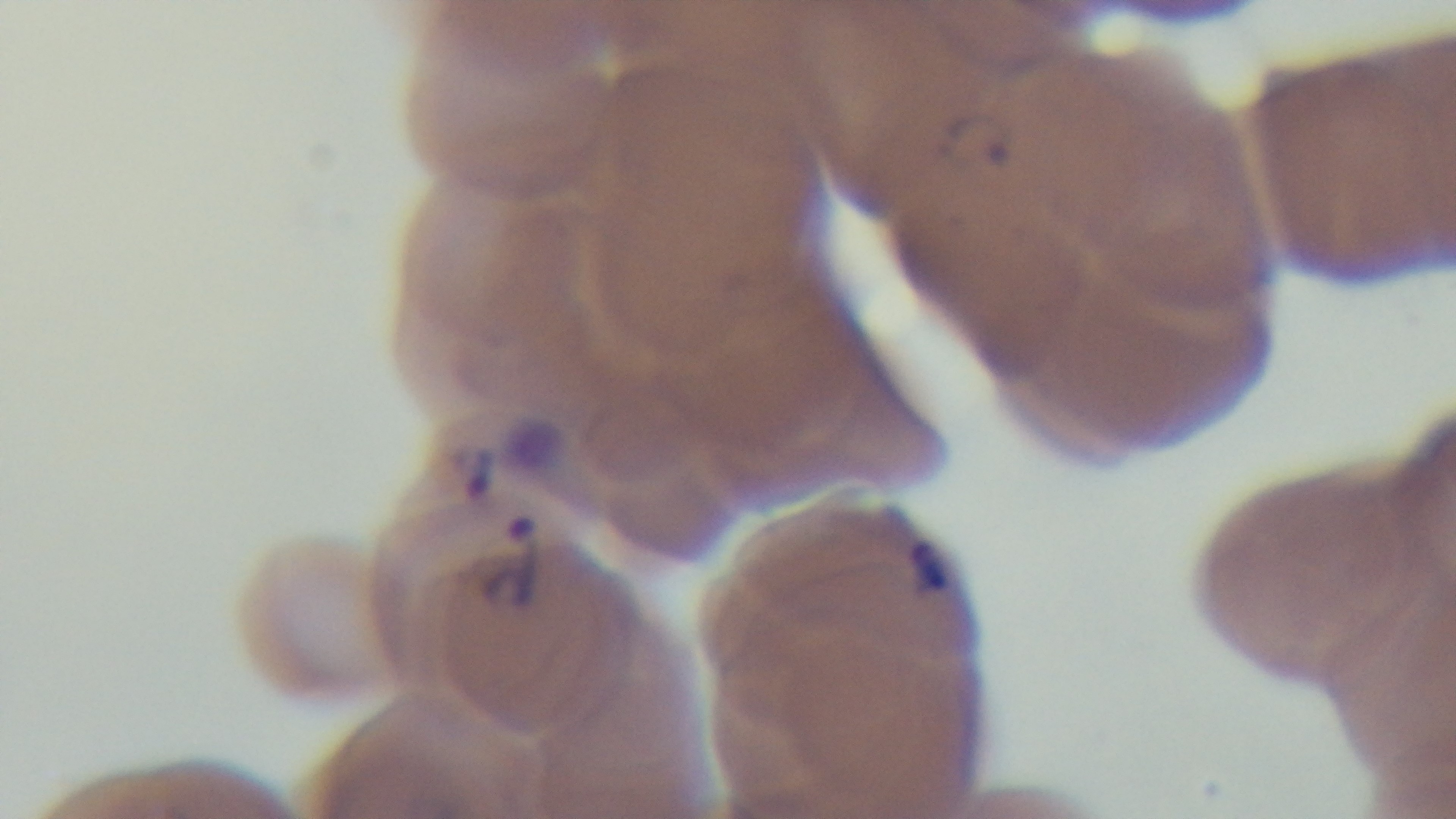 Giemsa stain. Photomicrograph. Malaria status: positive. Preparation: thin blood film. 100x oil-immersion objective. Captured with a mounted 4K digital camera. One field from the slide.